Name the parasite shown.
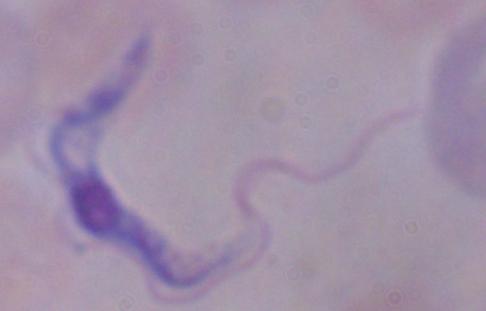
A trypanosome.

Captured at 1000x magnification. Micrograph.